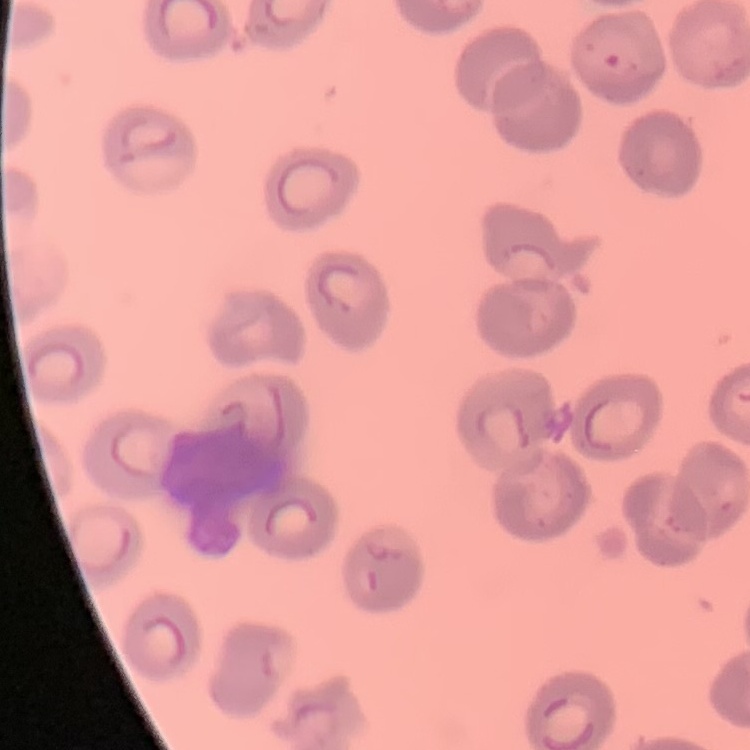
Summary:
  - Red blood cell morphology: no rouleaux formation
  - Preparation: thin blood smear
  - Stain: Field's or Giemsa
  - Image type: one tile cut from a larger photomicrograph